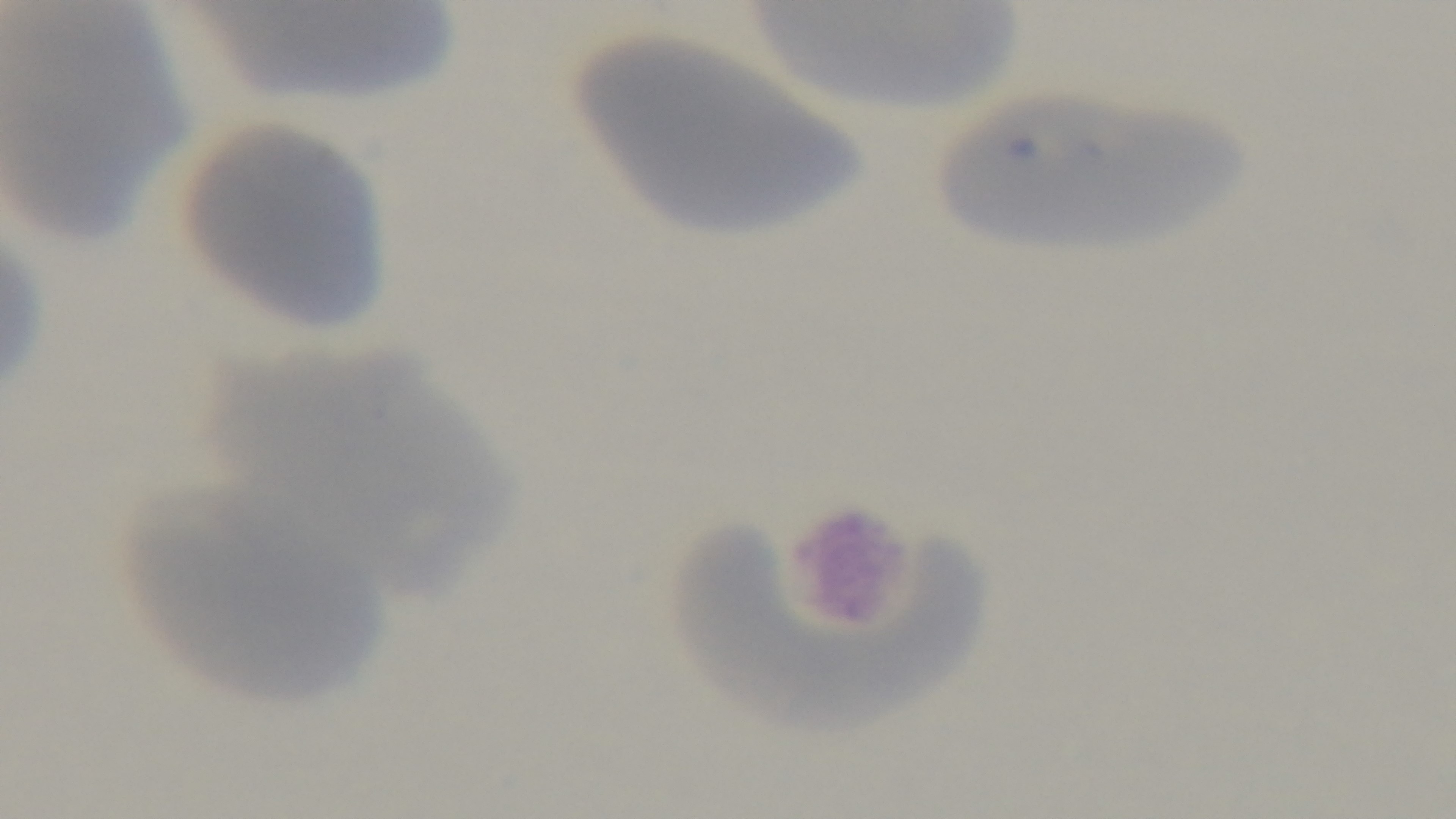
capture = mounted 4K digital camera
stain = Giemsa
malaria status = negative
field of view = one from the slide
preparation = thin
modality = light microscopy
objective = 100x oil immersion